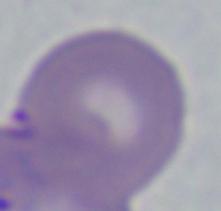
A Babesia parasite is seen. Photomicrograph. Captured at 1000x magnification.